Name the cell type shown.
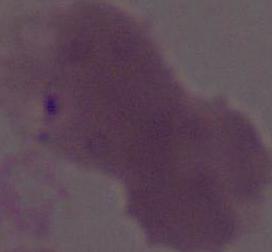

An erythrocyte.

magnification = 1000x
modality = photomicrograph